Outline each blood parasite and name the species.
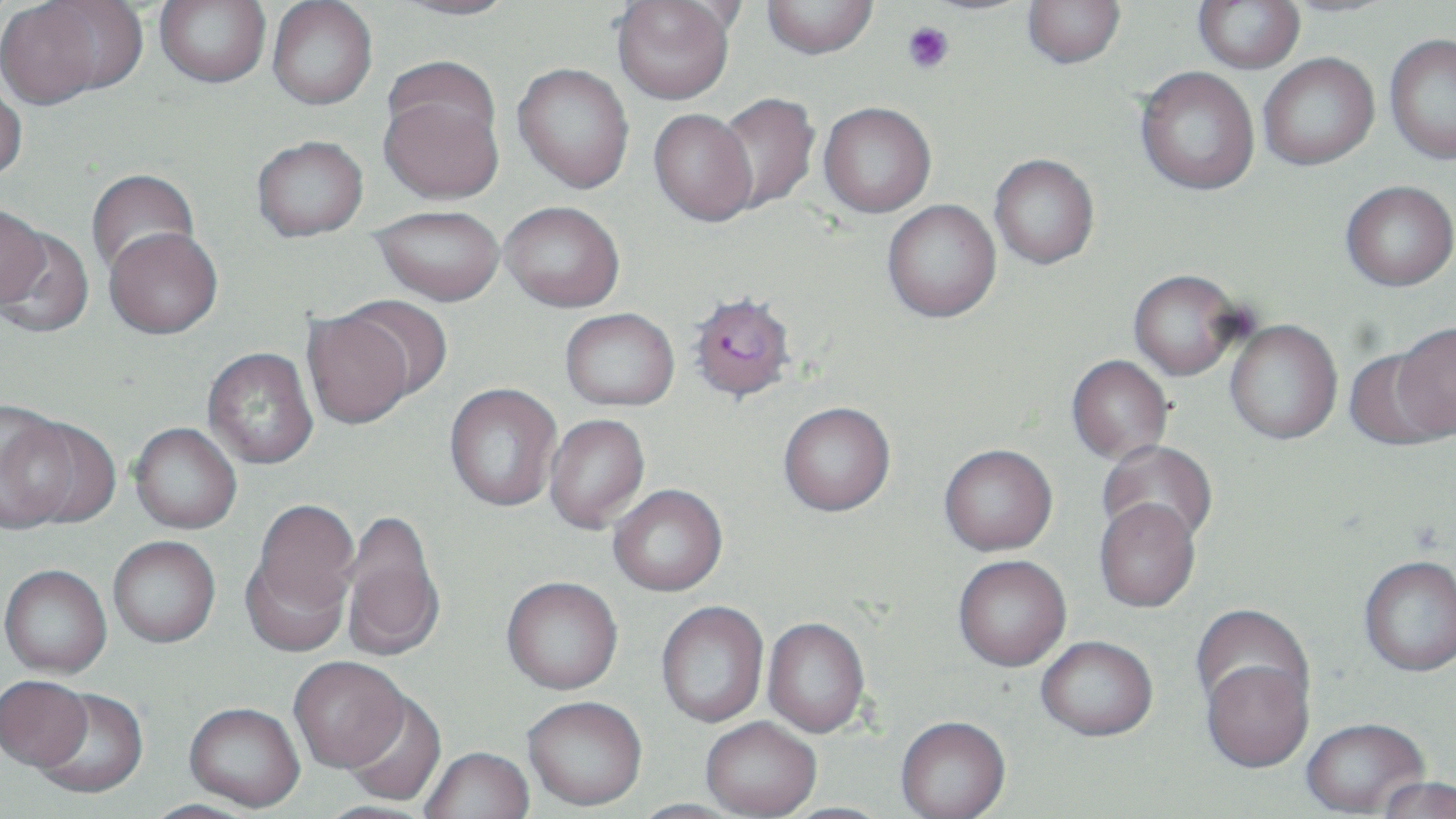

Approximate bounding boxes as (x1, y1, x2, y2) in pixels.
Plasmodium falciparum-infected red blood cells: (686, 291, 796, 403).
No Plasmodium ovale, Plasmodium malariae, Plasmodium vivax, Babesia divergens, or Trypanosoma brucei observed.

Summary:
  - Platelet locations: (902, 21, 955, 74)
  - Uninfected red blood cell locations: (154, 0, 271, 88), (390, 0, 522, 20), (761, 0, 878, 59), (1023, 0, 1125, 68), (1193, 0, 1305, 74), (0, 1, 121, 108), (267, 1, 378, 110), (612, 1, 736, 104), (1384, 33, 1456, 165), (1258, 53, 1379, 170), (513, 63, 634, 194), (1135, 66, 1260, 195), (378, 76, 504, 205), (0, 78, 27, 184), (714, 93, 820, 214), (818, 102, 936, 218), (649, 109, 758, 226), (251, 136, 368, 241), (989, 153, 1099, 269), (84, 169, 200, 279), (1341, 180, 1455, 291), (882, 199, 1001, 323), (500, 201, 625, 312), (0, 204, 50, 309), (371, 205, 504, 305), (104, 227, 223, 339), (0, 228, 94, 339), (1128, 269, 1245, 380), (340, 295, 454, 404), (560, 308, 679, 410), (302, 309, 415, 429), (1224, 319, 1342, 446), (1388, 322, 1456, 443), (202, 348, 318, 469), (1343, 349, 1449, 452), (1066, 355, 1173, 465), (444, 383, 561, 512), (778, 401, 896, 517), (0, 407, 86, 535), (545, 414, 650, 534), (129, 422, 242, 534), (1098, 441, 1217, 549), (939, 445, 1058, 558), (608, 486, 727, 597), (247, 499, 359, 632), (1094, 500, 1201, 614), (339, 509, 445, 662), (108, 536, 221, 648), (953, 557, 1072, 674), (1358, 559, 1456, 679), (0, 566, 112, 679), (501, 577, 623, 694), (656, 602, 769, 728), (1191, 603, 1312, 721), (763, 619, 869, 739), (1036, 639, 1158, 745), (289, 657, 409, 774), (1200, 657, 1315, 776), (0, 677, 93, 774), (32, 690, 149, 800), (340, 693, 446, 807), (523, 699, 647, 813), (183, 704, 304, 813), (701, 720, 821, 819), (895, 720, 1011, 819), (1301, 721, 1429, 818), (420, 749, 535, 819), (1377, 778, 1455, 819), (139, 800, 259, 819), (627, 800, 747, 819), (311, 801, 440, 819), (777, 802, 902, 819)
  - Slide-level diagnosis: Plasmodium falciparum
  - Preparation: thin blood smear
  - Magnification: 1000x
  - Field of view: one of a larger specimen
  - Modality: light microscopy
  - Stain: May-Grünwald-Giemsa
  - Image size: 1456×819 pixels